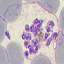
Summary:
  - Malaria status: parasitized
  - Capture: smartphone through the microscope eyepiece
  - Image type: automatically extracted cell patch, resized to 64 × 64 pixels
  - Stain: Giemsa
  - Preparation: thin smear